Locate every blood parasite and identify its species.
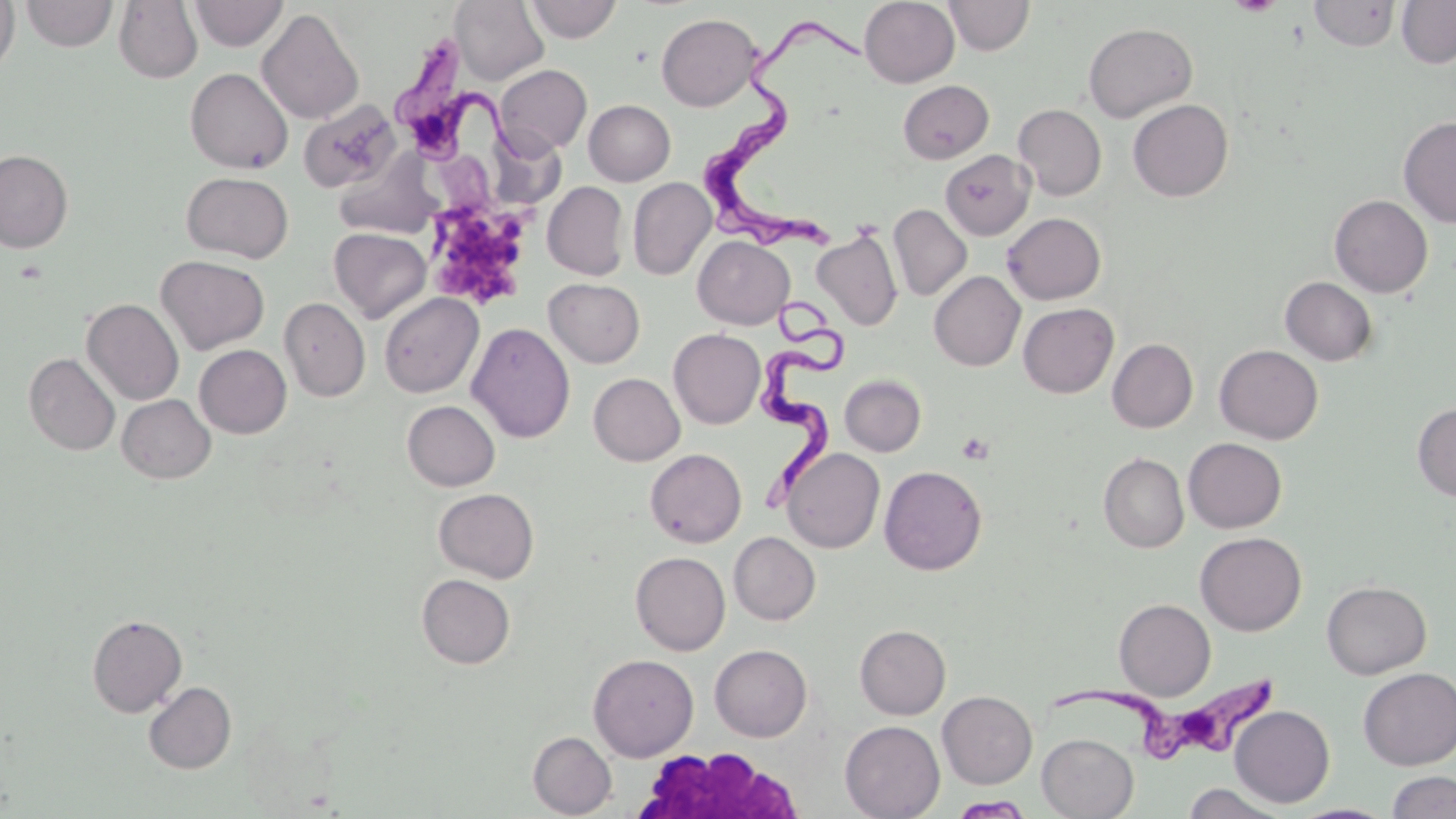
Approximate bounding boxes as named x1/y1/x2/y2 corners in pixels.
Trypanosoma brucei: (x1=704, y1=17, x2=874, y2=253), (x1=397, y1=37, x2=525, y2=166), (x1=753, y1=286, x2=851, y2=519), (x1=1050, y1=674, x2=1287, y2=761).
No Plasmodium falciparum, Plasmodium ovale, Plasmodium malariae, Plasmodium vivax, or Babesia divergens observed.

Summary:
  - Uninfected red blood cell locations: (x1=0, y1=0, x2=19, y2=78), (x1=189, y1=0, x2=288, y2=50), (x1=525, y1=0, x2=622, y2=43), (x1=859, y1=0, x2=960, y2=87), (x1=944, y1=0, x2=1034, y2=56), (x1=1397, y1=0, x2=1456, y2=68), (x1=20, y1=1, x2=118, y2=51), (x1=113, y1=1, x2=203, y2=84), (x1=450, y1=1, x2=548, y2=85), (x1=1309, y1=1, x2=1400, y2=51), (x1=257, y1=8, x2=364, y2=125), (x1=656, y1=12, x2=762, y2=111), (x1=1083, y1=22, x2=1197, y2=122), (x1=495, y1=64, x2=591, y2=156), (x1=185, y1=67, x2=293, y2=174), (x1=898, y1=80, x2=993, y2=163), (x1=1127, y1=99, x2=1233, y2=201), (x1=584, y1=100, x2=675, y2=185), (x1=299, y1=101, x2=400, y2=193), (x1=1013, y1=104, x2=1106, y2=200), (x1=1398, y1=116, x2=1456, y2=227), (x1=1, y1=149, x2=73, y2=253), (x1=940, y1=150, x2=1035, y2=241), (x1=331, y1=151, x2=441, y2=240), (x1=181, y1=172, x2=294, y2=263), (x1=628, y1=177, x2=716, y2=279), (x1=542, y1=182, x2=629, y2=280), (x1=1329, y1=195, x2=1433, y2=297), (x1=888, y1=204, x2=972, y2=301), (x1=1001, y1=213, x2=1106, y2=305), (x1=329, y1=227, x2=431, y2=322), (x1=812, y1=227, x2=903, y2=331), (x1=693, y1=235, x2=794, y2=329), (x1=156, y1=255, x2=269, y2=354), (x1=929, y1=271, x2=1025, y2=370), (x1=1281, y1=277, x2=1378, y2=365), (x1=544, y1=278, x2=645, y2=367), (x1=379, y1=292, x2=483, y2=398), (x1=279, y1=297, x2=370, y2=401), (x1=82, y1=298, x2=184, y2=405), (x1=1018, y1=302, x2=1118, y2=398), (x1=467, y1=322, x2=575, y2=443), (x1=668, y1=329, x2=766, y2=429), (x1=1107, y1=338, x2=1197, y2=433), (x1=194, y1=344, x2=291, y2=438), (x1=1214, y1=344, x2=1324, y2=444), (x1=24, y1=353, x2=120, y2=456), (x1=589, y1=373, x2=685, y2=465), (x1=840, y1=374, x2=926, y2=456), (x1=117, y1=394, x2=216, y2=483), (x1=402, y1=400, x2=500, y2=491), (x1=1412, y1=403, x2=1456, y2=501), (x1=1184, y1=438, x2=1286, y2=533), (x1=782, y1=447, x2=885, y2=553), (x1=645, y1=448, x2=746, y2=547), (x1=1098, y1=452, x2=1189, y2=552), (x1=879, y1=465, x2=987, y2=575), (x1=433, y1=488, x2=539, y2=582), (x1=729, y1=532, x2=820, y2=625), (x1=1195, y1=532, x2=1307, y2=635), (x1=631, y1=551, x2=730, y2=655), (x1=416, y1=573, x2=515, y2=669), (x1=1322, y1=580, x2=1431, y2=679), (x1=1113, y1=598, x2=1215, y2=700), (x1=86, y1=614, x2=187, y2=716), (x1=855, y1=625, x2=951, y2=719), (x1=709, y1=644, x2=812, y2=741), (x1=588, y1=653, x2=698, y2=761), (x1=1358, y1=667, x2=1456, y2=770), (x1=144, y1=681, x2=236, y2=773), (x1=937, y1=691, x2=1037, y2=788), (x1=1229, y1=705, x2=1335, y2=807), (x1=840, y1=720, x2=945, y2=819), (x1=528, y1=731, x2=617, y2=817), (x1=1037, y1=733, x2=1138, y2=818), (x1=1386, y1=771, x2=1456, y2=819), (x1=1182, y1=783, x2=1290, y2=818), (x1=948, y1=795, x2=1035, y2=818)
  - White blood cell locations: (x1=637, y1=747, x2=810, y2=819)
  - Platelet locations: (x1=1229, y1=0, x2=1281, y2=15), (x1=434, y1=203, x2=531, y2=302), (x1=956, y1=432, x2=994, y2=464)
  - Slide-level diagnosis: Trypanosoma brucei
  - Modality: light microscopy
  - Image size: 1456×819 pixels
  - Preparation: thin blood film
  - Field of view: one of a larger specimen
  - Stain: May-Grünwald-Giemsa
  - Magnification: 1000x